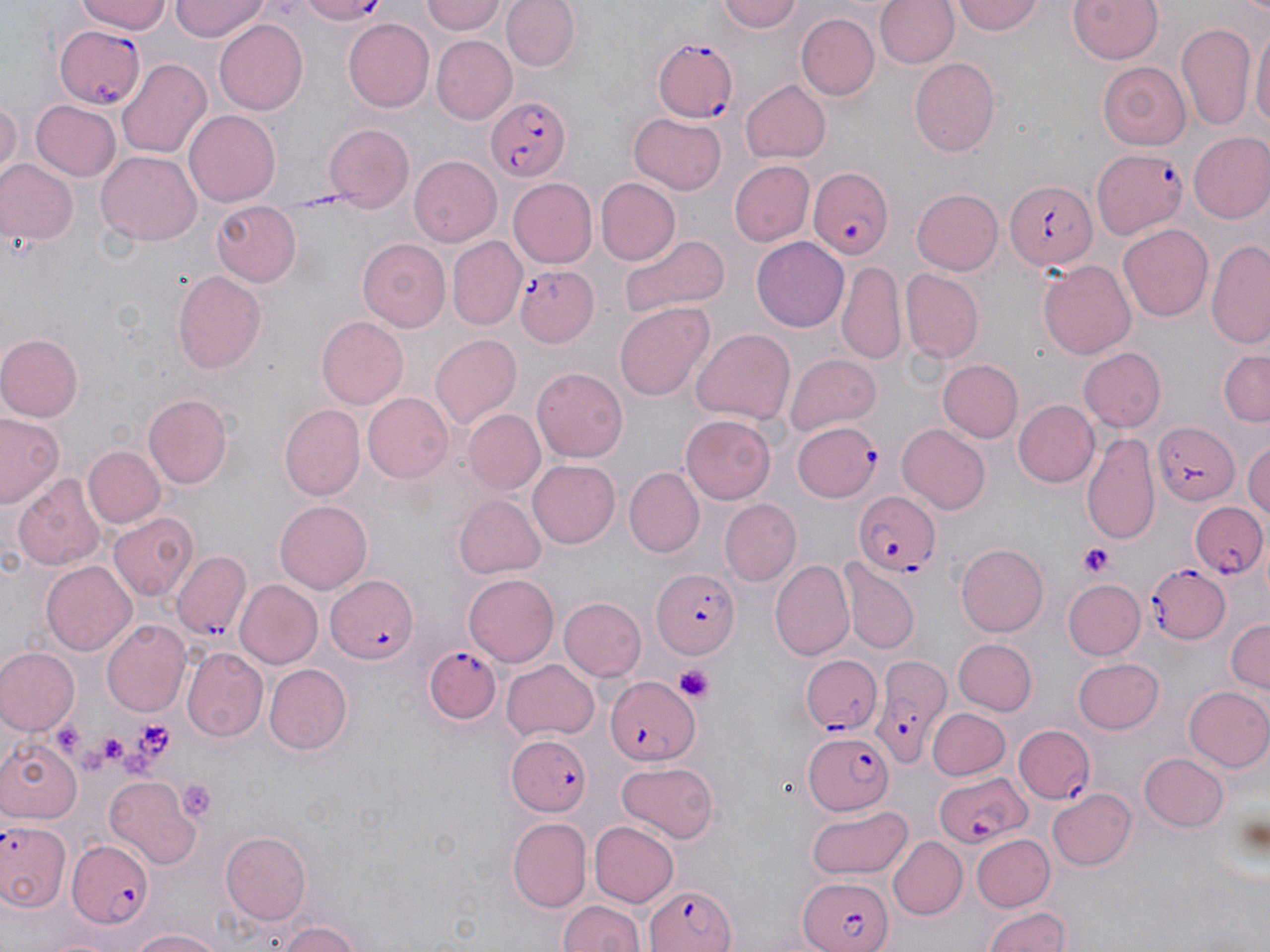

Summary:
  - Coordinate format: approximate bounding boxes as (x1,y1)-(x2,y2) corner pairs in pixels
  - Platelet locations: (1077,543)-(1118,578), (673,665)-(714,702), (128,718)-(177,762), (96,731)-(144,772), (176,780)-(217,824)
  - Plasmodium falciparum-infected red blood cell locations: (292,0)-(390,24), (53,24)-(148,108), (653,38)-(741,124), (484,95)-(571,183), (1091,148)-(1186,242), (806,168)-(894,261), (1006,182)-(1096,271), (517,265)-(597,347), (793,421)-(881,501), (1152,422)-(1240,506), (852,490)-(941,577), (1189,501)-(1270,581), (172,552)-(252,643), (1147,562)-(1231,646), (650,567)-(738,660), (326,574)-(422,662), (427,645)-(504,723), (800,653)-(882,734), (869,656)-(948,768), (607,673)-(703,765), (1010,722)-(1099,807), (507,733)-(591,816), (802,733)-(895,815), (936,772)-(1030,849), (0,818)-(70,917), (64,840)-(156,925), (797,876)-(893,952), (640,884)-(738,951)
  - Uninfected red blood cell locations: (79,0)-(170,34), (170,0)-(272,41), (424,0)-(507,36), (715,0)-(804,34), (874,0)-(956,70), (953,0)-(1048,36), (1066,0)-(1164,65), (503,1)-(579,73), (426,4)-(508,68), (795,12)-(881,100), (343,18)-(434,110), (215,19)-(309,113), (1176,21)-(1257,132), (1250,28)-(1269,139), (432,38)-(516,121), (118,57)-(212,161), (910,57)-(1001,155), (1100,62)-(1193,150), (739,79)-(829,163), (0,96)-(21,181), (30,100)-(121,181), (186,111)-(281,206), (629,112)-(727,193), (325,123)-(415,214), (1187,133)-(1270,223), (97,151)-(201,245), (409,156)-(501,248), (0,160)-(77,245), (728,160)-(813,248), (509,178)-(597,268), (596,178)-(680,264), (911,188)-(1004,277), (211,200)-(301,288), (1119,222)-(1212,320), (618,233)-(728,319), (356,236)-(453,332), (752,236)-(849,328), (447,238)-(525,330), (1205,239)-(1270,349), (1038,260)-(1135,360), (837,262)-(906,366), (171,269)-(268,373), (901,270)-(983,362), (615,302)-(715,400), (316,317)-(407,408), (692,328)-(797,426), (429,333)-(521,430), (0,334)-(81,422), (1077,347)-(1164,432), (1218,349)-(1270,426), (785,352)-(882,437), (939,359)-(1023,443), (533,365)-(629,460), (361,392)-(453,483), (143,394)-(233,488), (1011,399)-(1098,488), (279,404)-(365,500), (463,409)-(545,495), (0,413)-(62,507), (682,416)-(775,503), (897,424)-(992,514), (1083,429)-(1162,547), (1243,442)-(1270,521), (83,445)-(163,530), (528,459)-(620,549), (624,467)-(703,555), (11,474)-(105,572), (453,495)-(545,579), (275,499)-(372,594), (720,499)-(800,584), (108,511)-(198,602), (956,543)-(1048,636), (840,557)-(919,655), (772,559)-(855,662), (42,561)-(136,655), (463,573)-(559,666), (1062,579)-(1145,661), (233,580)-(322,669), (559,596)-(646,680), (104,618)-(190,715), (1226,618)-(1269,697), (951,638)-(1036,716), (183,648)-(267,740), (0,649)-(78,736), (1072,656)-(1163,734), (502,660)-(599,741), (263,663)-(353,755), (1184,685)-(1270,773), (928,708)-(1010,780), (0,738)-(79,824), (1138,753)-(1227,832), (616,762)-(718,845), (105,776)-(199,867), (1047,788)-(1136,871), (806,804)-(913,881), (507,818)-(592,911), (587,820)-(678,908), (219,831)-(311,925), (888,835)-(967,920), (971,835)-(1053,912), (557,898)-(644,952), (981,904)-(1074,952), (272,918)-(367,951), (126,927)-(228,952)
  - Slide-level diagnosis: Plasmodium falciparum
  - Field of view: one of a larger specimen
  - Preparation: thin blood smear
  - Image size: 1270×952 pixels
  - Stain: May-Grünwald-Giemsa
  - Magnification: 1000x
  - Modality: light microscopy